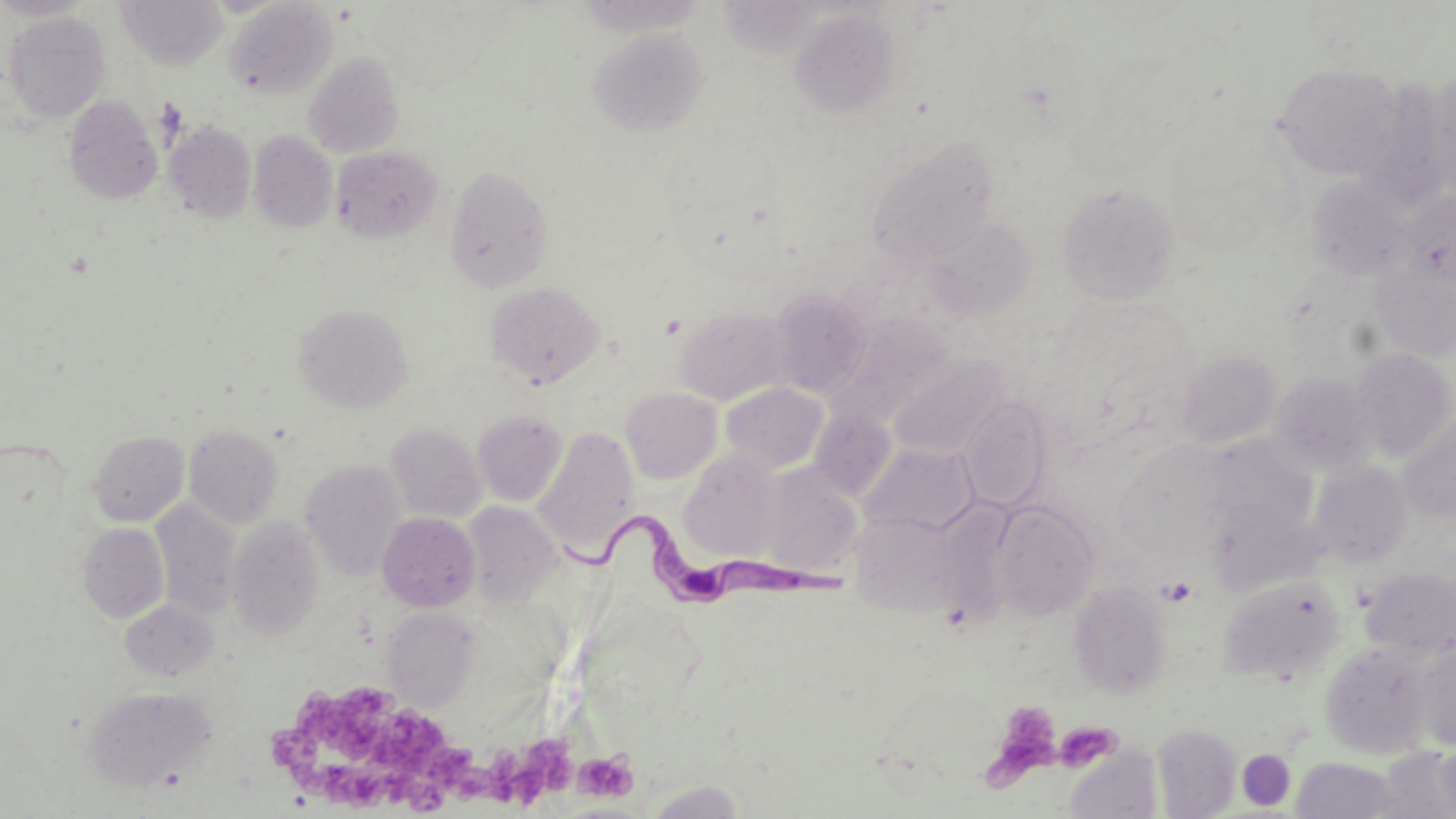
slide-level diagnosis = Trypanosoma brucei
field of view = single
platelet locations = approximate bounding boxes as named x1/y1/x2/y2 corners in pixels: (x1=1159, y1=577, x2=1196, y2=607), (x1=272, y1=686, x2=503, y2=813), (x1=989, y1=701, x2=1063, y2=780), (x1=1051, y1=722, x2=1120, y2=773), (x1=507, y1=737, x2=578, y2=805), (x1=573, y1=751, x2=638, y2=802)
image size = 1456×819 pixels
stain = May-Grünwald-Giemsa
preparation = thin blood smear
uninfected red blood cell locations = approximate bounding boxes as named x1/y1/x2/y2 corners in pixels: (x1=0, y1=0, x2=95, y2=20), (x1=114, y1=1, x2=228, y2=70), (x1=224, y1=1, x2=337, y2=99), (x1=790, y1=9, x2=901, y2=119), (x1=3, y1=10, x2=111, y2=123), (x1=588, y1=28, x2=708, y2=137), (x1=303, y1=52, x2=404, y2=158), (x1=1273, y1=63, x2=1405, y2=180), (x1=1425, y1=67, x2=1456, y2=195), (x1=64, y1=96, x2=163, y2=204), (x1=164, y1=121, x2=257, y2=224), (x1=248, y1=130, x2=338, y2=233), (x1=866, y1=138, x2=999, y2=266), (x1=330, y1=146, x2=442, y2=243), (x1=445, y1=164, x2=554, y2=293), (x1=1306, y1=174, x2=1413, y2=282), (x1=1058, y1=183, x2=1180, y2=303), (x1=1399, y1=192, x2=1456, y2=291), (x1=924, y1=218, x2=1035, y2=322), (x1=1370, y1=260, x2=1456, y2=360), (x1=484, y1=280, x2=606, y2=387), (x1=769, y1=289, x2=872, y2=398), (x1=294, y1=303, x2=414, y2=412), (x1=675, y1=306, x2=792, y2=406), (x1=1350, y1=347, x2=1456, y2=461), (x1=1176, y1=350, x2=1282, y2=449), (x1=887, y1=355, x2=1007, y2=459), (x1=1270, y1=371, x2=1378, y2=475), (x1=721, y1=383, x2=829, y2=475), (x1=620, y1=387, x2=722, y2=483), (x1=961, y1=397, x2=1050, y2=511), (x1=808, y1=409, x2=898, y2=502), (x1=472, y1=410, x2=568, y2=506), (x1=1398, y1=414, x2=1456, y2=522), (x1=384, y1=423, x2=486, y2=522), (x1=184, y1=424, x2=284, y2=528), (x1=532, y1=427, x2=640, y2=560), (x1=89, y1=429, x2=190, y2=526), (x1=1202, y1=435, x2=1316, y2=538), (x1=860, y1=442, x2=980, y2=536), (x1=1114, y1=444, x2=1231, y2=559), (x1=679, y1=449, x2=782, y2=560), (x1=300, y1=458, x2=407, y2=581), (x1=1309, y1=460, x2=1413, y2=568), (x1=758, y1=464, x2=864, y2=578), (x1=1207, y1=496, x2=1319, y2=596), (x1=150, y1=500, x2=240, y2=619), (x1=461, y1=501, x2=562, y2=606), (x1=990, y1=501, x2=1100, y2=620), (x1=848, y1=508, x2=977, y2=619), (x1=377, y1=511, x2=480, y2=612), (x1=226, y1=515, x2=325, y2=642), (x1=79, y1=524, x2=170, y2=623), (x1=1360, y1=566, x2=1456, y2=661), (x1=1218, y1=575, x2=1346, y2=684), (x1=1068, y1=581, x2=1171, y2=698), (x1=120, y1=598, x2=219, y2=682), (x1=382, y1=608, x2=479, y2=710), (x1=1410, y1=640, x2=1456, y2=751), (x1=1320, y1=643, x2=1432, y2=760), (x1=83, y1=686, x2=217, y2=791), (x1=1152, y1=725, x2=1241, y2=818), (x1=1437, y1=740, x2=1456, y2=815), (x1=1237, y1=742, x2=1295, y2=809), (x1=1063, y1=746, x2=1162, y2=819), (x1=1375, y1=747, x2=1456, y2=817), (x1=1292, y1=757, x2=1399, y2=818), (x1=644, y1=781, x2=747, y2=819)
Trypanosoma brucei locations = approximate bounding boxes as named x1/y1/x2/y2 corners in pixels: (x1=562, y1=510, x2=849, y2=616)
magnification = 1000x
modality = light microscopy